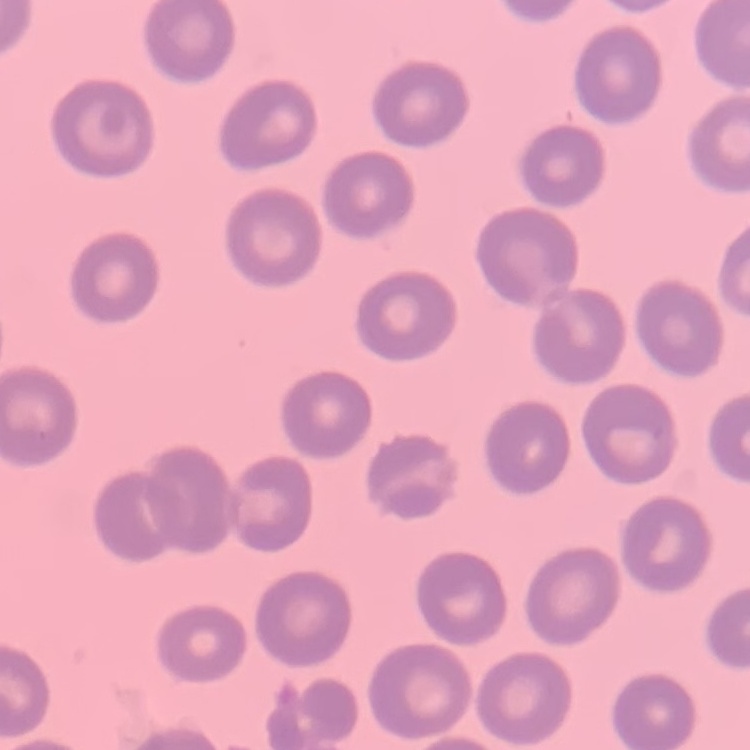
Summary:
  - Red blood cell morphology: no rouleaux formation
  - Image type: square crop of a larger photomicrograph
  - Preparation: thin blood smear
  - Stain: Field's or Giemsa